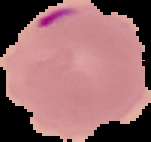
The area outside the segmented cell region is set to black. Image is 151×142 pixels. From a thin blood film. Result: malaria parasites detected.